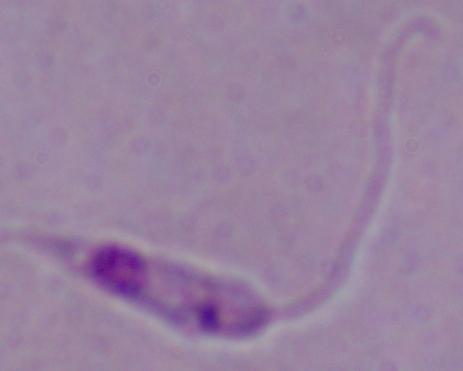
Summary:
  - Magnification: 1000x
  - Identification: Leishmania
  - Modality: micrograph